State which parasite is depicted.
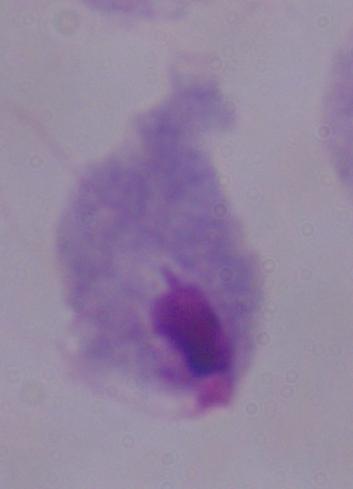

A trichomonad.

Summary:
  - Magnification: 1000x
  - Modality: photomicrograph